Classify this cell by malaria status.
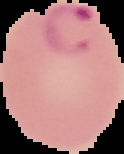

It is parasitized.

Image is 124×154 pixels. From a thin blood smear. Cell region segmented out of the field of view; the surrounding area is masked to black.